Locate every leukocyte (white blood cell).
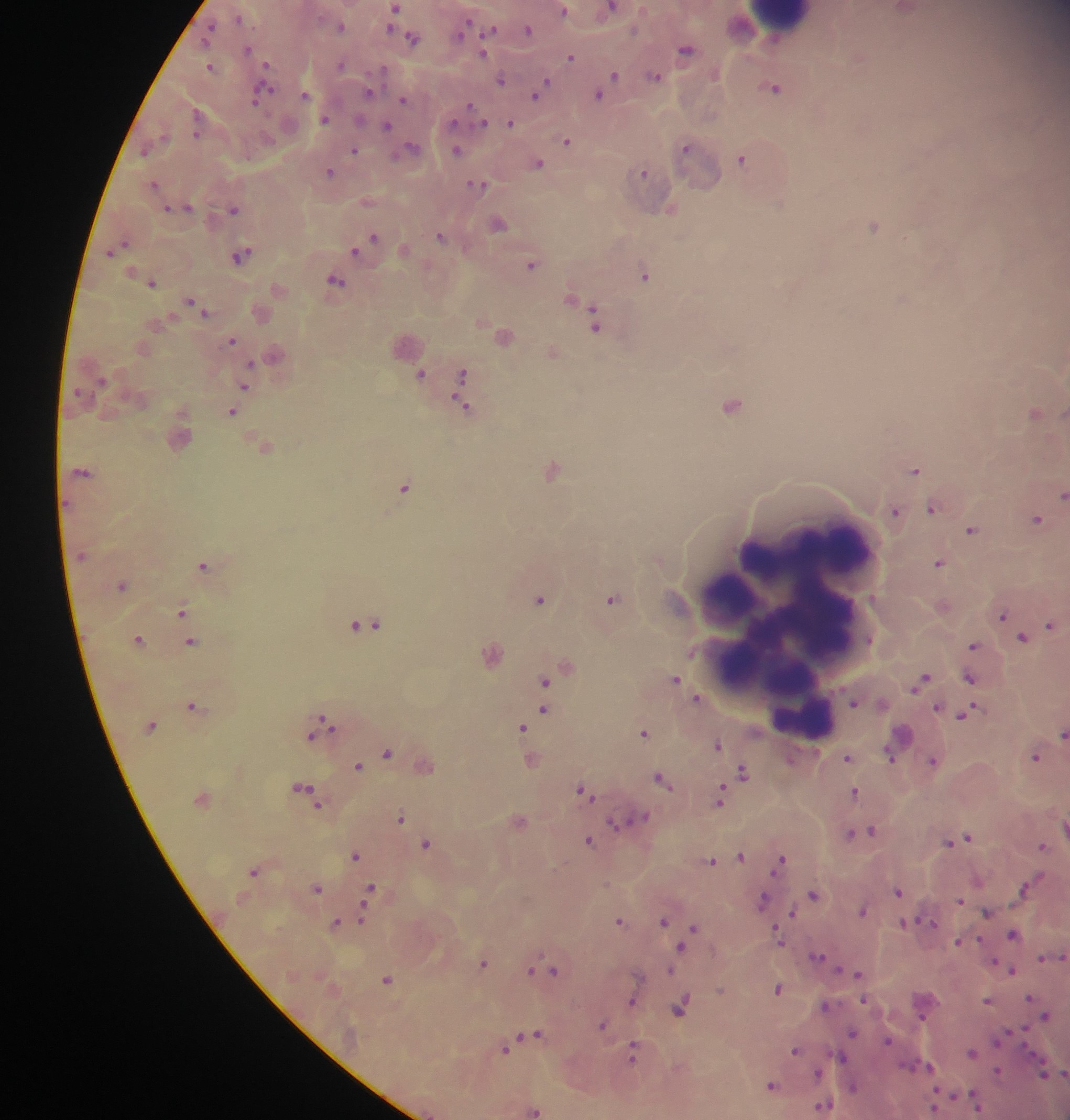
Approximate centers as x y in pixels.
Leukocytes: 781 17; 788 621.

country = Ghana
Plasmodium parasite locations = approximate centers as x y in pixels: 394 8; 611 8; 905 9; 562 11; 392 15; 238 18; 210 26; 340 27; 463 28; 390 29; 492 30; 527 30; 633 31; 413 39; 247 49; 685 51; 482 54; 569 56; 266 64; 340 65; 209 67; 614 76; 654 76; 500 81; 602 88; 774 89; 261 93; 368 93; 538 93; 304 95; 598 96; 403 100; 470 106; 195 114; 324 119; 482 123; 510 123; 387 126; 195 135; 566 141; 685 147; 353 150; 456 150; 143 152; 741 159; 538 164; 330 172; 642 172; 477 184; 153 185; 187 207; 166 208; 233 209; 497 224; 872 226; 440 236; 373 237; 354 252; 241 255; 531 265; 644 276; 335 280; 151 283; 189 302; 205 312; 592 319; 232 341; 249 365; 420 374; 461 374; 244 386; 462 394; 731 405; 232 412; 1033 412; 551 471; 913 471; 82 472; 404 486; 1061 495; 66 503; 932 508; 894 511; 1035 519; 970 530; 938 564; 203 566; 121 586; 611 599; 539 600; 181 612; 1001 617; 366 625; 1049 625; 1022 638; 190 642; 973 645; 968 678; 674 679; 545 680; 920 680; 695 699; 853 702; 192 705; 936 707; 543 710; 966 713; 320 724; 520 727; 643 733; 1062 734; 716 745; 387 753; 888 756; 1034 757; 846 758; 933 761; 357 766; 742 772; 661 780; 724 786; 306 791; 584 791; 853 792; 718 800; 400 818; 639 819; 615 823; 1064 827; 868 831; 850 832; 966 838; 588 840; 950 842; 425 844; 1041 845; 355 855; 740 856; 710 861; 779 861; 253 871; 1021 887; 316 888; 370 889; 897 892; 812 894; 366 900; 762 900; 959 900; 862 911; 792 912; 986 913; 362 919; 618 921; 663 921; 927 921; 334 923; 903 923; 692 928; 1011 934; 777 937; 956 942; 680 948; 817 956; 1062 956; 1040 959; 482 963; 531 970; 553 970; 670 970; 838 970; 1011 970; 858 974; 387 979; 778 989; 1028 998; 864 1000; 986 1001; 630 1002; 824 1006; 680 1009; 1045 1015; 920 1017; 601 1025; 851 1032; 536 1033; 888 1041; 504 1049; 794 1050; 633 1053; 971 1053; 840 1057; 929 1067; 996 1071; 816 1074; 1043 1074; 1063 1074; 770 1086; 852 1087; 824 1104; 976 1105; 933 1108; 533 1110
preparation = thick blood film
image size = 1070×1120 pixels
capture = mobile-phone photograph through a microscope
field of view = single